Identify the blood parasite species.
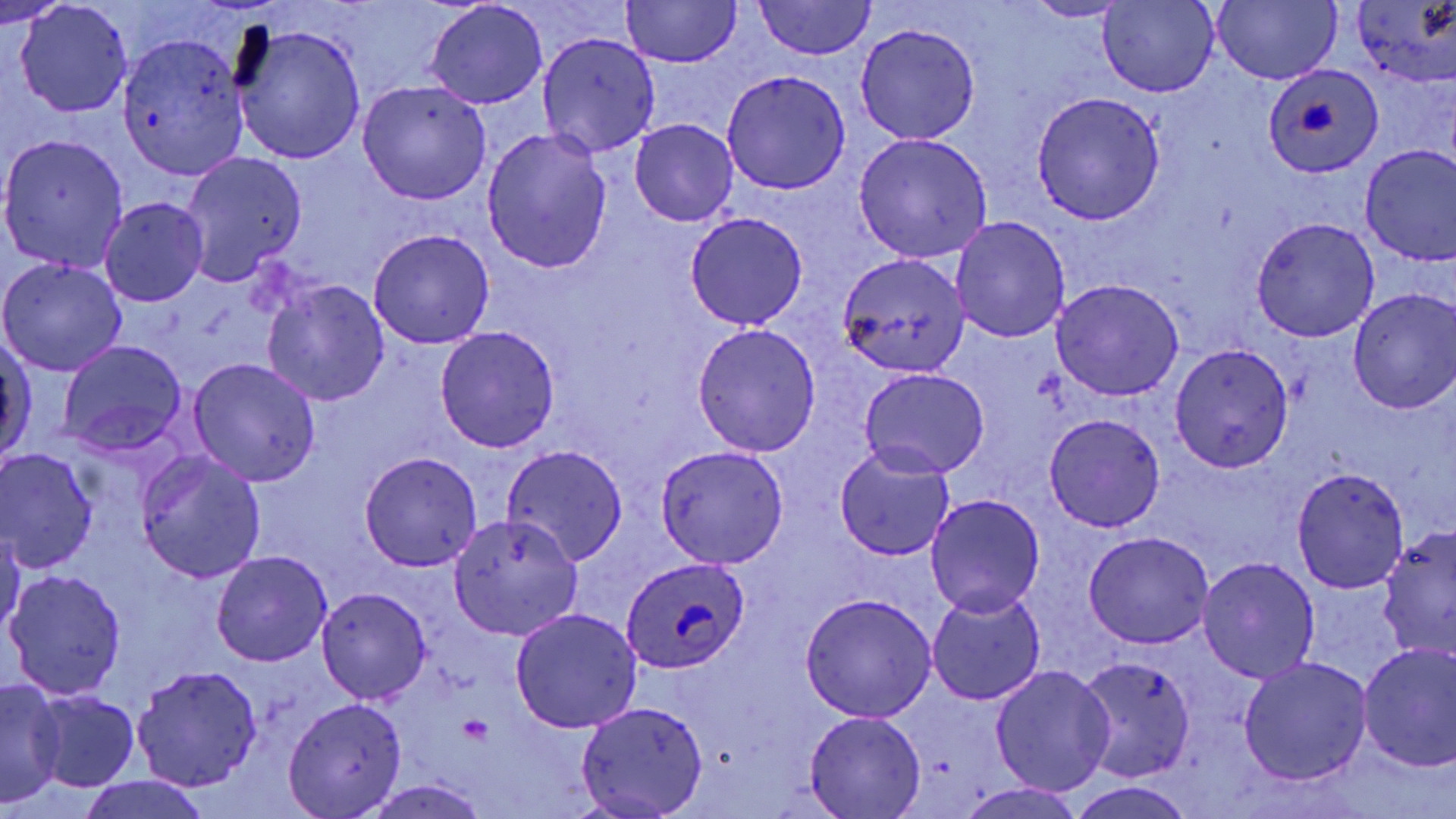
Plasmodium ovale.

{
  "uninfected_red_blood_cell_locations": "approximate bounding boxes as (x1, y1, x2, y2) in pixels: (0, 0, 66, 28), (622, 0, 740, 68), (1211, 0, 1341, 86), (754, 1, 877, 60), (1098, 1, 1217, 97), (1351, 1, 1456, 88), (425, 2, 548, 108), (1021, 2, 1132, 22), (13, 3, 133, 116), (231, 21, 366, 165), (854, 24, 981, 145), (116, 32, 249, 181), (536, 32, 661, 158), (722, 69, 852, 193), (356, 80, 492, 205), (1032, 93, 1166, 226), (630, 121, 738, 226), (482, 128, 611, 274), (852, 133, 993, 264), (0, 134, 130, 269), (1359, 145, 1456, 263), (179, 151, 307, 287), (99, 197, 209, 307), (685, 213, 809, 331), (951, 216, 1071, 341), (1251, 217, 1380, 341), (369, 229, 494, 349), (836, 253, 969, 379), (0, 257, 128, 377), (263, 280, 390, 407), (1051, 280, 1185, 400), (1347, 288, 1456, 414), (691, 322, 822, 455), (435, 325, 561, 453), (1, 333, 37, 469), (56, 339, 189, 460), (1171, 343, 1295, 470), (187, 358, 321, 487), (858, 367, 991, 478), (1042, 415, 1165, 532), (501, 444, 628, 566), (833, 444, 957, 560), (654, 445, 789, 568), (0, 448, 98, 574), (136, 450, 266, 584), (359, 451, 483, 571), (1290, 465, 1410, 593), (925, 494, 1046, 617), (448, 516, 583, 641), (0, 527, 24, 641), (1377, 528, 1456, 660), (1082, 530, 1216, 649), (211, 550, 334, 668), (1196, 556, 1322, 683), (5, 570, 127, 700), (317, 587, 431, 703), (927, 591, 1046, 706), (800, 593, 936, 721), (509, 607, 642, 735), (1357, 642, 1456, 773), (1238, 655, 1373, 785), (1077, 657, 1195, 783), (988, 664, 1115, 795), (133, 665, 263, 791), (0, 679, 66, 806), (33, 691, 140, 791), (283, 697, 407, 817), (576, 699, 709, 816), (804, 711, 927, 819), (76, 775, 212, 819), (353, 779, 494, 819), (1070, 782, 1198, 819), (953, 784, 1087, 819)",
  "preparation": "thin blood smear",
  "magnification": "1000x",
  "stain": "May-Grünwald-Giemsa",
  "plasmodium_ovale_infected_red_blood_cell_locations": "approximate bounding boxes as (x1, y1, x2, y2) in pixels: (1264, 64, 1383, 180), (619, 556, 752, 673)",
  "image_size": "1456×819 pixels",
  "platelet_locations": "approximate bounding boxes as (x1, y1, x2, y2) in pixels: (457, 714, 491, 744)",
  "modality": "optical microscopy",
  "field_of_view": "single"
}